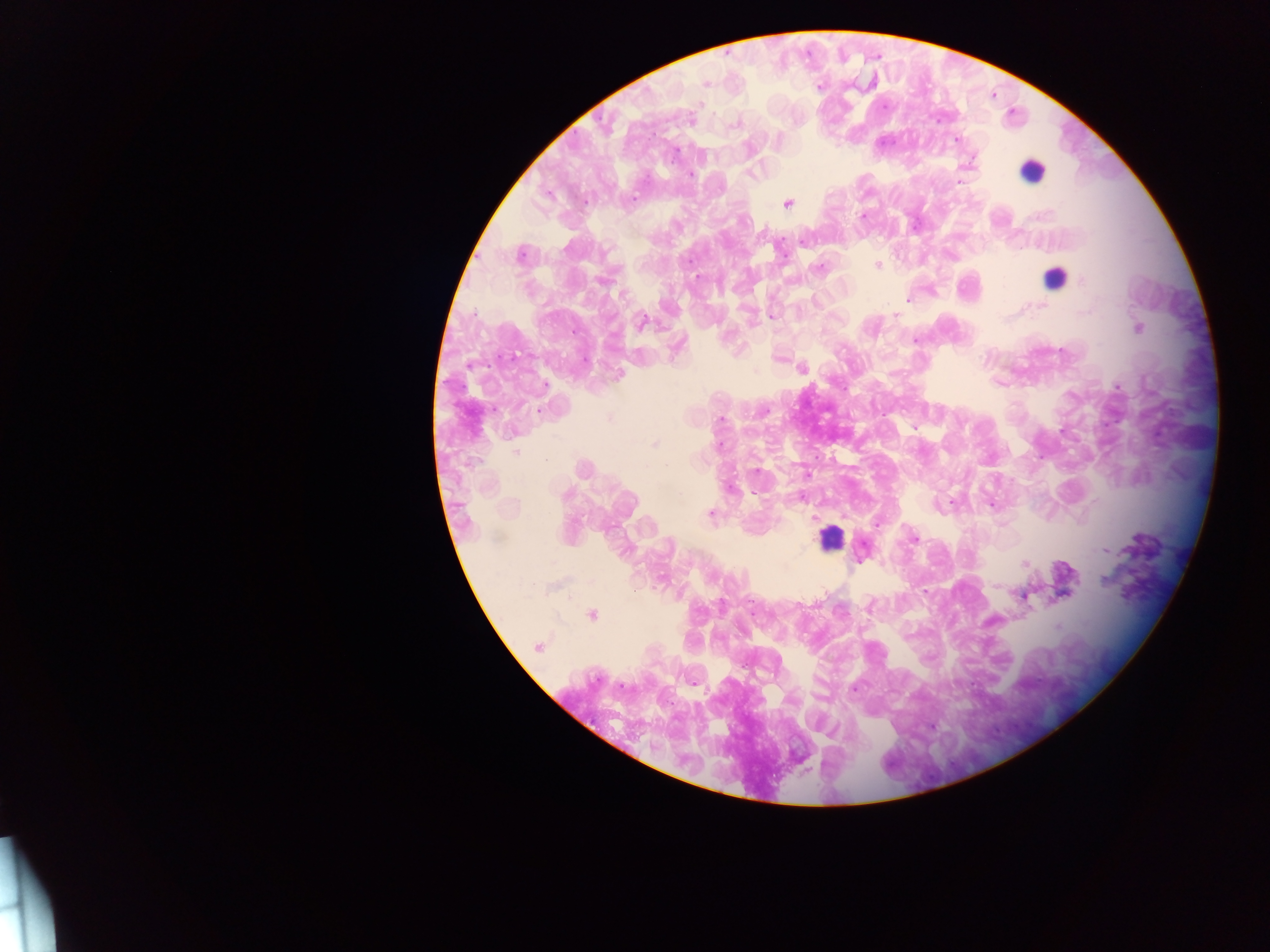

Approximate centers as [x, y] in pixels. Leukocyte locations: [1032, 171], [1054, 277], [829, 538]. Plasmodium parasite locations: [706, 84], [870, 84], [820, 86], [885, 107], [692, 119], [735, 125], [956, 140], [676, 153], [752, 174], [691, 175], [958, 182], [634, 198], [787, 203], [862, 216], [804, 241], [520, 255], [877, 266], [819, 268], [698, 278], [1083, 281], [907, 299], [1042, 306], [894, 316], [772, 317], [642, 322], [1139, 328], [916, 340], [802, 368], [619, 374], [546, 385], [1117, 387], [765, 411], [539, 412], [609, 418], [720, 420], [914, 428], [654, 445], [719, 445], [515, 451], [666, 465], [583, 469], [757, 471], [807, 474], [730, 489], [754, 493], [566, 495], [951, 503], [992, 504], [710, 513], [815, 518], [876, 523], [914, 539], [1105, 551], [1025, 563], [1104, 580], [1024, 597], [592, 615], [1058, 627], [538, 647], [855, 689]. Single field of view. Collected in Ghana. Image is 1270×952 pixels. Photographed through a microscope with a mobile-phone camera. Thick blood film.